Report the malaria status of this cell.
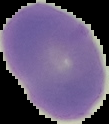

It is uninfected.

preparation = thin blood smear
image type = segmented cell region on a black background
image size = 109×124 pixels